Look for Plasmodium parasites.
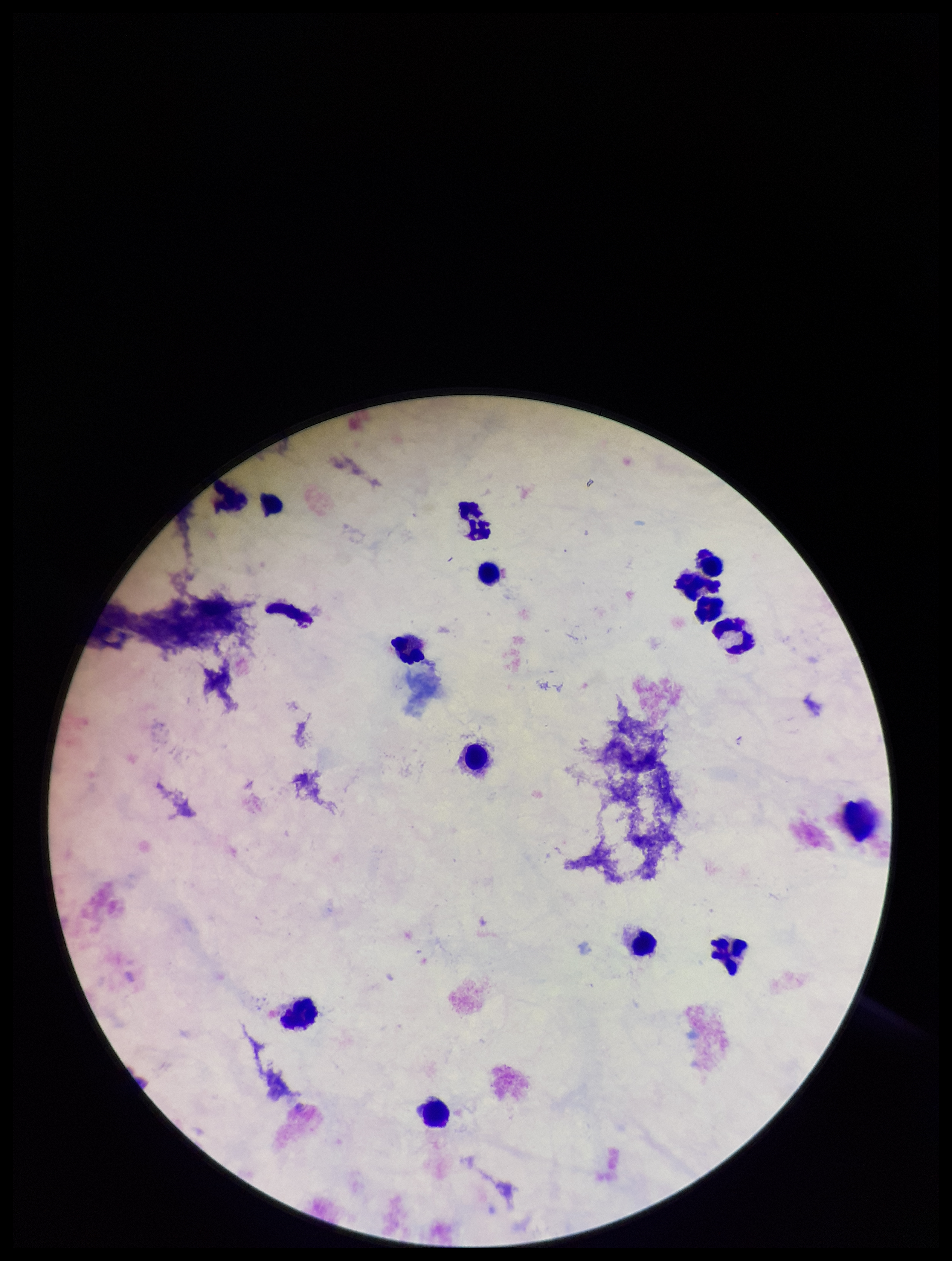
None detected.

Leukocyte count: 14. Parasite count: 0. Stained with Giemsa. Preparation: thick blood smear. Image is 952×1261 pixels. Patient malaria status: negative. One field from this slide. Smartphone photograph taken through the eyepiece of a microscope.